Assess this cell for malaria.
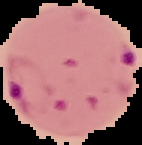

It is parasitized.

Image is 142×145 pixels. From a thin blood smear. Cell region segmented out of the field of view; the surrounding area is masked to black.